Locate every blood parasite and identify its species.
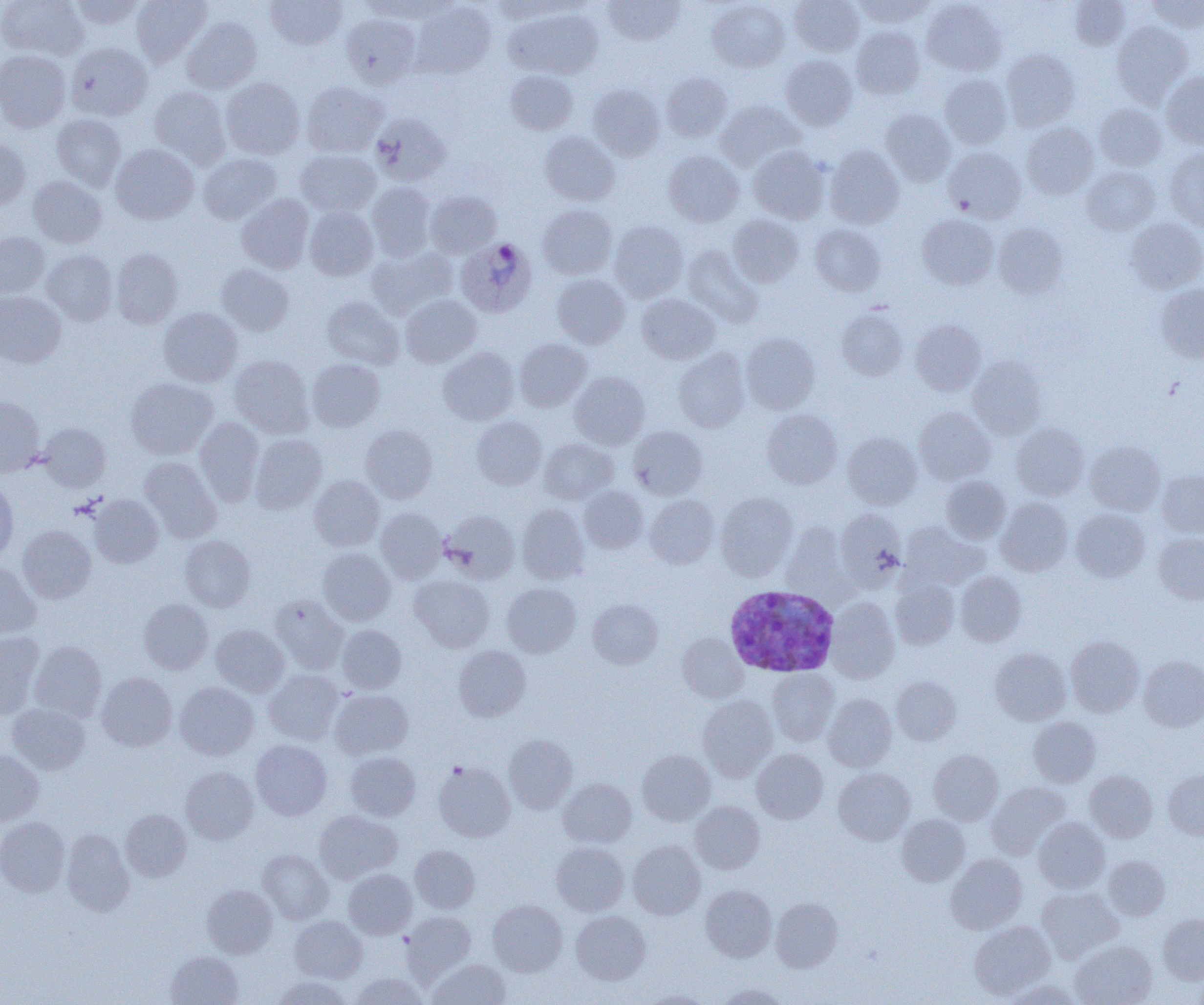

Approximate bounding boxes as (x1, y1, x2, y2) in pixels.
Plasmodium ovale-infected red blood cells: (454, 237, 532, 320), (724, 585, 840, 678).
No Plasmodium falciparum, Plasmodium malariae, Plasmodium vivax, Babesia divergens, or Trypanosoma brucei observed.

Uninfected red blood cell locations: (0, 0, 88, 61), (69, 0, 145, 29), (131, 0, 212, 66), (265, 0, 347, 50), (356, 0, 444, 20), (603, 0, 685, 45), (707, 0, 790, 72), (790, 0, 864, 57), (854, 0, 933, 27), (1069, 0, 1129, 49), (1146, 0, 1204, 32), (490, 1, 576, 22), (922, 1, 1007, 75), (411, 2, 495, 79), (504, 7, 603, 79), (340, 13, 421, 88), (181, 17, 262, 94), (1112, 21, 1193, 107), (851, 26, 924, 99), (65, 42, 153, 121), (1002, 49, 1079, 131), (0, 50, 70, 133), (780, 55, 857, 130), (506, 70, 578, 135), (662, 72, 732, 142), (1161, 72, 1204, 148), (940, 74, 1012, 149), (220, 77, 305, 159), (302, 81, 387, 157), (588, 83, 665, 160), (149, 86, 231, 169), (715, 100, 806, 171), (1094, 103, 1166, 170), (881, 109, 955, 186), (370, 113, 451, 186), (52, 114, 126, 191), (1022, 122, 1098, 199), (540, 131, 620, 206), (0, 139, 30, 210), (110, 144, 199, 225), (825, 145, 904, 229), (748, 146, 829, 224), (943, 147, 1026, 222), (295, 149, 381, 216), (1165, 149, 1204, 230), (664, 151, 744, 226), (199, 153, 281, 224), (1082, 165, 1160, 235), (28, 176, 107, 248), (366, 182, 436, 261), (425, 190, 501, 258), (236, 194, 315, 274), (538, 204, 617, 279), (304, 206, 378, 280), (917, 214, 999, 289), (728, 215, 803, 287), (1126, 218, 1204, 293), (609, 220, 688, 302), (993, 223, 1067, 298), (810, 224, 885, 296), (0, 232, 49, 299), (682, 244, 761, 326), (366, 247, 456, 319), (111, 248, 183, 329), (42, 249, 118, 325), (216, 263, 294, 336), (551, 273, 630, 349), (1156, 284, 1204, 363), (0, 291, 66, 368), (637, 293, 720, 364), (400, 295, 481, 368), (323, 296, 405, 369), (158, 307, 242, 387), (837, 307, 907, 381), (910, 320, 985, 395), (741, 332, 820, 414), (514, 338, 592, 412), (438, 347, 519, 425), (673, 348, 749, 432), (229, 355, 314, 438), (968, 356, 1046, 439), (307, 358, 385, 431), (570, 371, 649, 450), (125, 377, 217, 460), (0, 395, 45, 477), (914, 407, 995, 484), (762, 409, 842, 489), (472, 416, 546, 490), (195, 417, 264, 507), (38, 422, 110, 491), (1011, 423, 1089, 500), (360, 424, 438, 503), (628, 426, 707, 499), (842, 432, 922, 509), (250, 433, 327, 513), (539, 438, 618, 504), (1085, 440, 1165, 515), (139, 456, 221, 542), (1157, 470, 1204, 537), (309, 475, 384, 551), (940, 475, 1011, 544), (0, 481, 18, 565), (579, 486, 648, 553), (716, 492, 798, 580), (88, 495, 163, 568), (645, 495, 719, 568), (996, 498, 1073, 576), (517, 503, 589, 584), (376, 507, 447, 583), (835, 509, 907, 590), (1071, 509, 1150, 582), (441, 510, 520, 583), (900, 521, 986, 591), (781, 523, 850, 598), (17, 525, 96, 603), (1154, 533, 1204, 604), (180, 535, 256, 611), (318, 547, 396, 625), (0, 564, 41, 639), (955, 571, 1027, 646), (410, 575, 494, 652), (890, 578, 960, 648), (502, 583, 581, 657), (270, 594, 348, 673), (826, 597, 900, 684), (138, 598, 213, 674), (588, 599, 663, 669), (211, 624, 289, 697), (337, 625, 406, 693), (0, 632, 44, 720), (677, 633, 747, 702), (1066, 636, 1144, 717), (29, 640, 107, 722), (453, 646, 531, 721), (990, 647, 1070, 725), (1139, 655, 1204, 731), (768, 669, 840, 746), (264, 670, 343, 744), (96, 672, 177, 751), (891, 676, 961, 745), (175, 682, 259, 761), (330, 689, 414, 759), (823, 694, 896, 771), (698, 695, 778, 781), (7, 703, 91, 774), (1028, 716, 1101, 786), (504, 735, 577, 813), (251, 740, 332, 820), (637, 749, 716, 825), (751, 749, 828, 824), (928, 749, 1003, 825), (0, 750, 44, 825), (345, 752, 420, 820), (433, 762, 515, 842), (181, 766, 258, 844), (833, 768, 915, 845), (1164, 769, 1204, 840), (1085, 770, 1157, 842), (558, 778, 636, 847), (987, 781, 1070, 858), (691, 801, 765, 874), (120, 809, 191, 881), (314, 810, 402, 883), (896, 814, 970, 886), (0, 817, 69, 897), (1033, 817, 1109, 892), (62, 829, 135, 916), (628, 841, 705, 919), (551, 842, 628, 915), (410, 845, 480, 913), (258, 849, 333, 924), (945, 854, 1027, 934), (1104, 855, 1171, 920), (343, 869, 417, 939), (202, 884, 277, 958), (700, 885, 777, 962), (1036, 887, 1122, 961), (770, 897, 843, 972), (487, 899, 567, 976), (402, 911, 476, 982), (571, 911, 650, 984), (1158, 912, 1204, 984), (289, 915, 367, 982), (969, 921, 1056, 999), (1070, 940, 1157, 1005), (165, 951, 243, 1005), (427, 958, 511, 1005), (351, 973, 429, 1005), (271, 976, 353, 1004), (1004, 980, 1083, 1005), (716, 983, 790, 1005), (641, 990, 715, 1004). Slide-level diagnosis: Plasmodium ovale. Light microscopy. Image is 1204×1005 pixels. Thin blood smear. One field of a larger specimen. 1000x magnification.